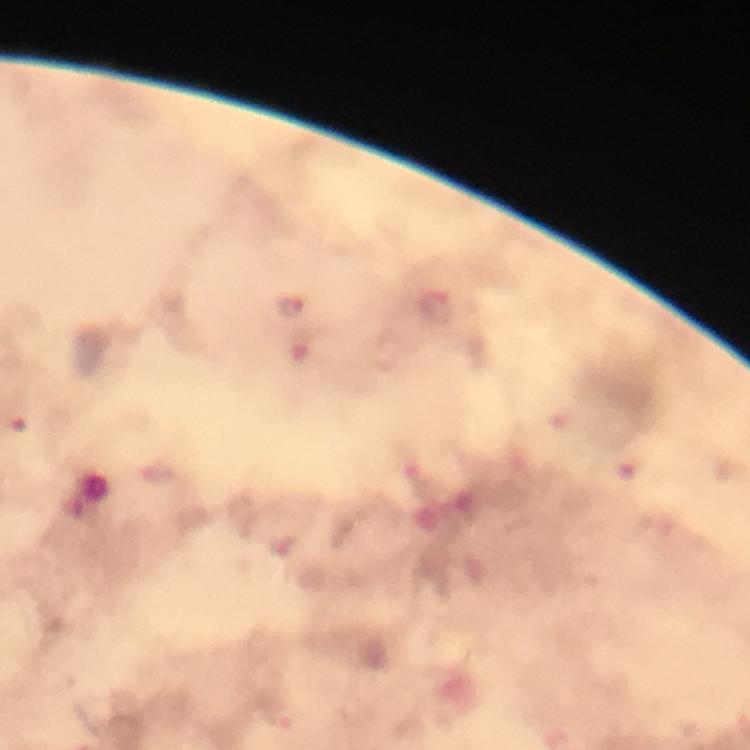
Approximate centers as (x, y) in pixels.
Summary:
  - Plasmodium parasite locations: (436, 307), (291, 308)
  - Preparation: thick blood smear
  - Stain: Giemsa
  - Cropped from: one field of view
  - Image size: 750×750 pixels
  - Magnification: 100x
  - Context: from a malaria diagnostic workup
  - Capture: smartphone camera through the microscope
  - Immersion oil: applied